Report the malaria status.
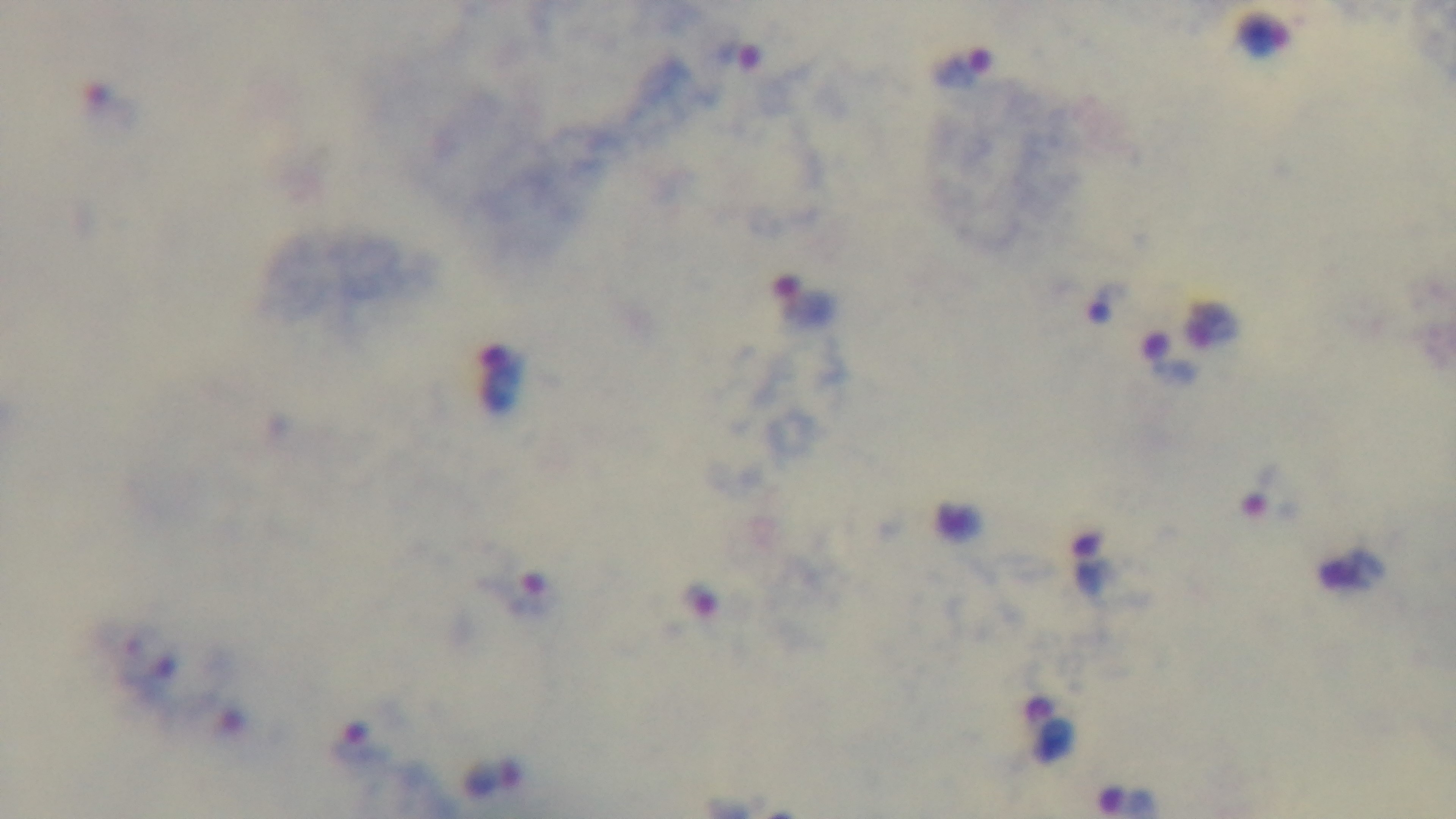
Infected.

Light microscopy. Mounted 4K digital camera. Giemsa stain. One field from the slide. Preparation: thick. Oil-immersion objective, 100x.